Assess this cell for malaria.
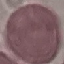

It is uninfected.

stain = Giemsa
image type = automatically extracted cell patch, resized to 64 × 64 pixels
preparation = thin blood smear
capture = smartphone camera at the microscope eyepiece